Locate every Plasmodium falciparum-infected red blood cell.
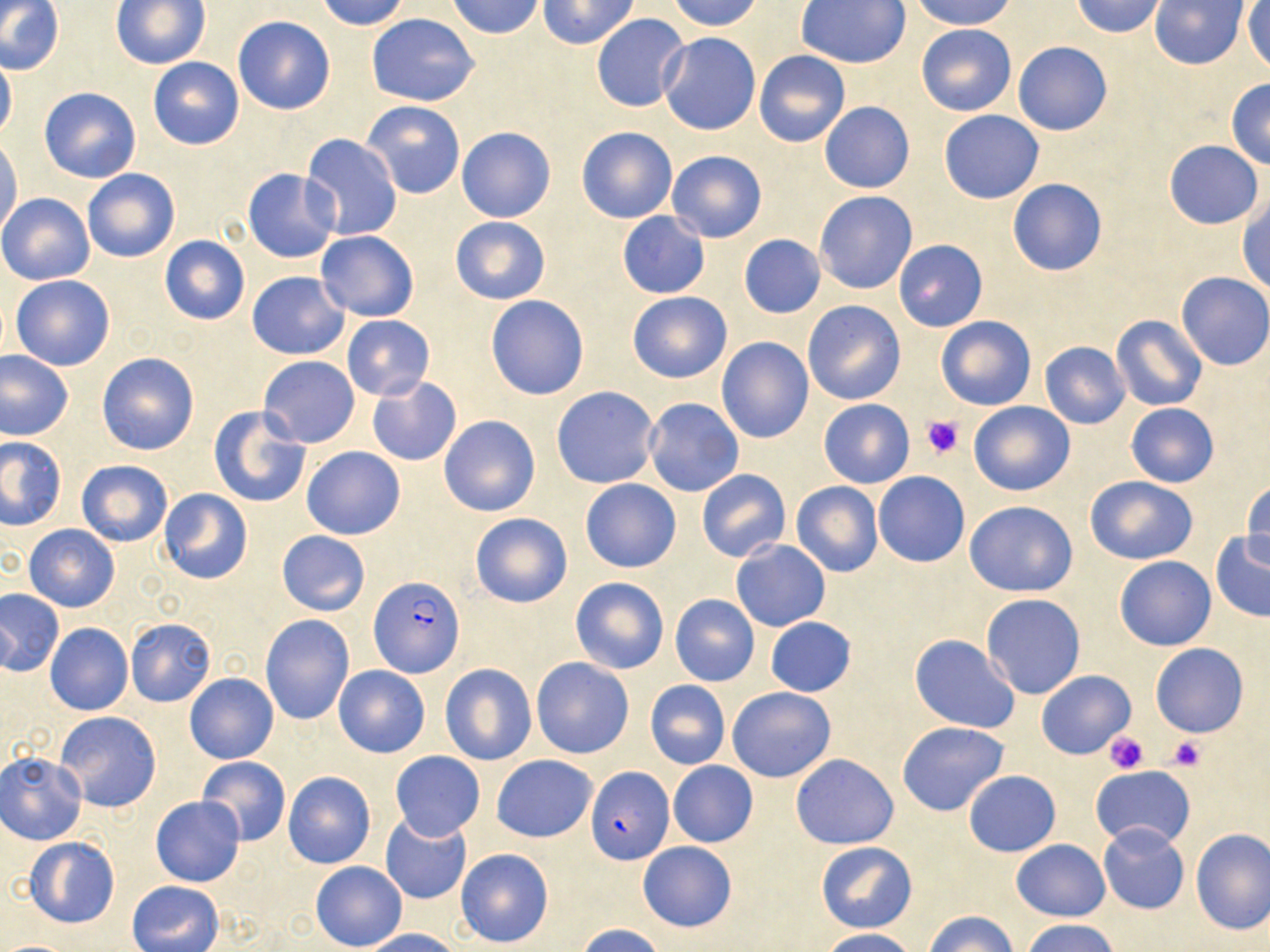

Approximate bounding boxes as named x1/y1/x2/y2 corners in pixels.
Plasmodium falciparum-infected red blood cells: (x1=369, y1=576, x2=466, y2=677), (x1=585, y1=768, x2=672, y2=863).

Platelet locations: (x1=922, y1=415, x2=965, y2=459), (x1=1103, y1=731, x2=1151, y2=774), (x1=1166, y1=736, x2=1206, y2=772). Uninfected red blood cell locations: (x1=315, y1=0, x2=410, y2=30), (x1=446, y1=0, x2=546, y2=39), (x1=539, y1=0, x2=640, y2=49), (x1=667, y1=0, x2=763, y2=31), (x1=906, y1=0, x2=1017, y2=30), (x1=1071, y1=0, x2=1166, y2=38), (x1=1149, y1=0, x2=1248, y2=70), (x1=0, y1=1, x2=64, y2=76), (x1=111, y1=1, x2=209, y2=70), (x1=1243, y1=1, x2=1270, y2=71), (x1=795, y1=2, x2=910, y2=69), (x1=367, y1=13, x2=480, y2=106), (x1=591, y1=13, x2=692, y2=112), (x1=233, y1=15, x2=336, y2=115), (x1=915, y1=22, x2=1016, y2=116), (x1=657, y1=32, x2=760, y2=135), (x1=1012, y1=42, x2=1113, y2=136), (x1=0, y1=51, x2=16, y2=142), (x1=755, y1=51, x2=850, y2=147), (x1=147, y1=56, x2=244, y2=150), (x1=1226, y1=79, x2=1270, y2=169), (x1=39, y1=86, x2=142, y2=183), (x1=361, y1=100, x2=467, y2=200), (x1=819, y1=102, x2=914, y2=192), (x1=939, y1=110, x2=1045, y2=203), (x1=576, y1=126, x2=678, y2=223), (x1=456, y1=127, x2=555, y2=223), (x1=300, y1=133, x2=403, y2=242), (x1=1, y1=136, x2=22, y2=239), (x1=1164, y1=140, x2=1263, y2=229), (x1=666, y1=150, x2=768, y2=243), (x1=83, y1=168, x2=180, y2=263), (x1=243, y1=169, x2=340, y2=263), (x1=1007, y1=177, x2=1108, y2=277), (x1=814, y1=191, x2=918, y2=294), (x1=0, y1=193, x2=94, y2=285), (x1=1237, y1=194, x2=1269, y2=294), (x1=616, y1=211, x2=711, y2=298), (x1=450, y1=216, x2=550, y2=305), (x1=315, y1=230, x2=419, y2=322), (x1=738, y1=234, x2=825, y2=318), (x1=159, y1=235, x2=250, y2=325), (x1=893, y1=240, x2=987, y2=331), (x1=247, y1=272, x2=350, y2=359), (x1=1176, y1=272, x2=1270, y2=370), (x1=11, y1=273, x2=115, y2=371), (x1=626, y1=291, x2=731, y2=383), (x1=485, y1=294, x2=590, y2=400), (x1=802, y1=299, x2=906, y2=405), (x1=341, y1=315, x2=435, y2=401), (x1=1112, y1=315, x2=1207, y2=412), (x1=935, y1=316, x2=1036, y2=410), (x1=717, y1=337, x2=814, y2=444), (x1=1040, y1=340, x2=1131, y2=429), (x1=0, y1=349, x2=74, y2=441), (x1=97, y1=352, x2=199, y2=455), (x1=258, y1=355, x2=360, y2=449), (x1=367, y1=377, x2=461, y2=467), (x1=551, y1=386, x2=661, y2=489), (x1=643, y1=397, x2=745, y2=497), (x1=818, y1=398, x2=915, y2=487), (x1=968, y1=400, x2=1076, y2=496), (x1=1125, y1=403, x2=1219, y2=486), (x1=209, y1=405, x2=311, y2=509), (x1=439, y1=415, x2=540, y2=517), (x1=0, y1=437, x2=66, y2=530), (x1=302, y1=446, x2=405, y2=539), (x1=75, y1=460, x2=173, y2=548), (x1=696, y1=468, x2=792, y2=563), (x1=873, y1=472, x2=969, y2=567), (x1=1084, y1=475, x2=1198, y2=565), (x1=580, y1=479, x2=681, y2=573), (x1=1243, y1=481, x2=1270, y2=572), (x1=791, y1=482, x2=883, y2=577), (x1=158, y1=489, x2=253, y2=584), (x1=965, y1=500, x2=1078, y2=597), (x1=469, y1=512, x2=572, y2=608), (x1=25, y1=525, x2=120, y2=612), (x1=277, y1=530, x2=371, y2=616), (x1=1209, y1=530, x2=1270, y2=622), (x1=731, y1=540, x2=830, y2=631), (x1=1115, y1=555, x2=1216, y2=650), (x1=554, y1=576, x2=654, y2=756), (x1=570, y1=576, x2=670, y2=674), (x1=0, y1=589, x2=64, y2=675), (x1=670, y1=594, x2=760, y2=686), (x1=980, y1=594, x2=1087, y2=699), (x1=260, y1=614, x2=354, y2=725), (x1=764, y1=617, x2=857, y2=697), (x1=126, y1=619, x2=215, y2=706), (x1=45, y1=623, x2=134, y2=716), (x1=910, y1=635, x2=1019, y2=732), (x1=1150, y1=643, x2=1249, y2=738), (x1=530, y1=656, x2=634, y2=759), (x1=441, y1=664, x2=537, y2=766), (x1=332, y1=665, x2=430, y2=758), (x1=1038, y1=670, x2=1135, y2=757), (x1=185, y1=673, x2=278, y2=764), (x1=645, y1=680, x2=730, y2=770), (x1=727, y1=686, x2=836, y2=782), (x1=55, y1=711, x2=161, y2=812), (x1=897, y1=720, x2=1012, y2=817), (x1=0, y1=751, x2=87, y2=845), (x1=390, y1=751, x2=485, y2=842), (x1=492, y1=754, x2=597, y2=843), (x1=790, y1=754, x2=898, y2=849), (x1=197, y1=756, x2=291, y2=845), (x1=669, y1=761, x2=758, y2=848), (x1=1090, y1=765, x2=1195, y2=849), (x1=963, y1=770, x2=1060, y2=857), (x1=283, y1=771, x2=375, y2=869), (x1=151, y1=796, x2=245, y2=886), (x1=380, y1=813, x2=472, y2=905), (x1=1098, y1=823, x2=1189, y2=914), (x1=1190, y1=828, x2=1270, y2=935), (x1=25, y1=837, x2=120, y2=928), (x1=1010, y1=839, x2=1109, y2=921), (x1=815, y1=841, x2=918, y2=933), (x1=638, y1=842, x2=737, y2=932), (x1=456, y1=848, x2=555, y2=948), (x1=311, y1=861, x2=407, y2=950), (x1=128, y1=880, x2=224, y2=952), (x1=924, y1=910, x2=1020, y2=951), (x1=1022, y1=918, x2=1122, y2=952), (x1=575, y1=924, x2=668, y2=952), (x1=363, y1=928, x2=462, y2=952), (x1=815, y1=929, x2=919, y2=952). Slide-level diagnosis: Plasmodium falciparum. May-Grünwald-Giemsa-stained preparation. Image is 1270×952 pixels. Light microscopy. Single field of view. Thin blood film. 1000x magnification.